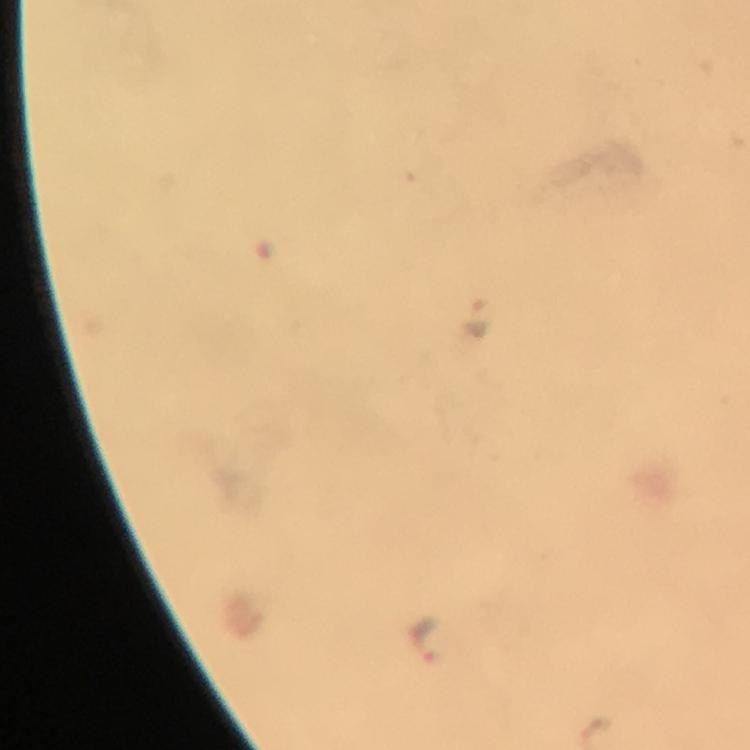
{
  "context": "from a diagnostic examination for malaria",
  "stain": "Giemsa",
  "preparation": "thick blood smear",
  "cropped_from": "a single field of view",
  "capture": "smartphone photograph through a microscope",
  "malaria_parasite_locations": "approximate object centers, in pixels from the top-left corner: (x=474, y=318), (x=426, y=640)",
  "magnification": "100x",
  "image_size": "750×750 pixels",
  "immersion_oil": "applied"
}